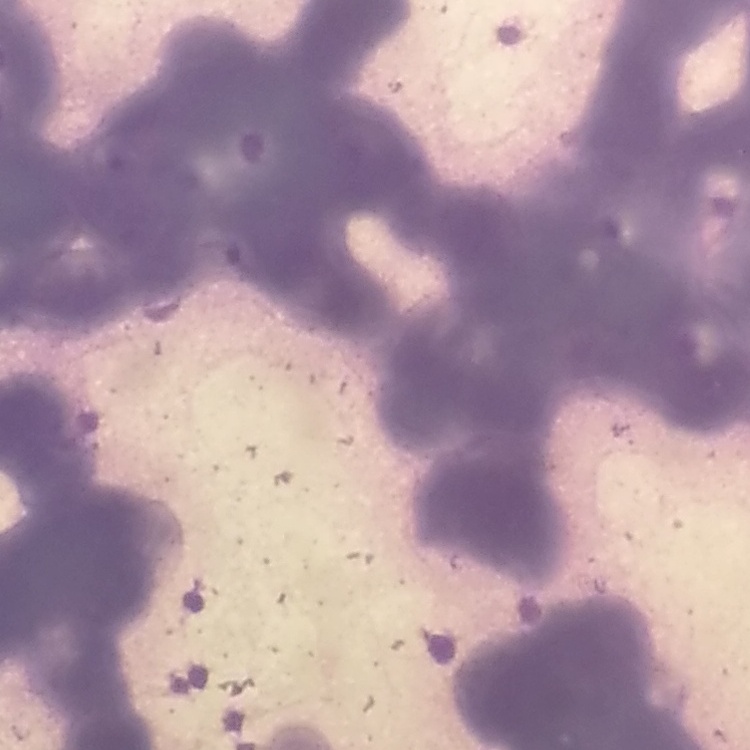
Summary:
  - Red blood cell morphology: rouleaux formation
  - Preparation: thin blood smear
  - Stain: Field's or Giemsa
  - Image type: square crop of a larger photomicrograph